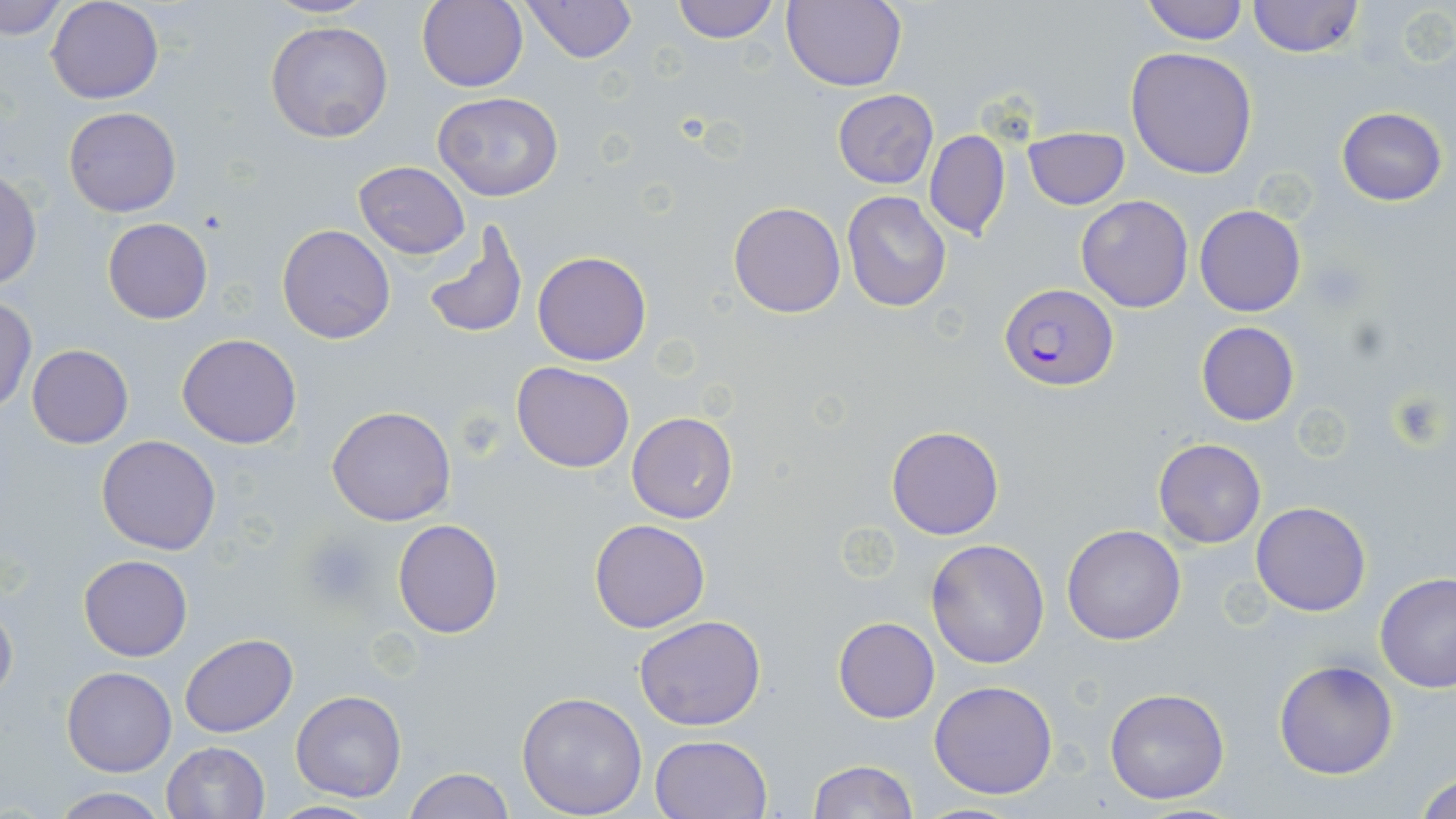
Summary:
  - Coordinate format: approximate bounding boxes as (x1,y1)-(x2,y2) corner pairs in pixels
  - Platelet locations: (1387,388)-(1451,450), (454,412)-(505,457), (303,534)-(375,606)
  - Uninfected red blood cell locations: (2,0)-(69,40), (46,0)-(164,104), (259,0)-(380,18), (415,0)-(529,90), (522,0)-(636,64), (672,0)-(780,44), (783,0)-(908,92), (1247,0)-(1363,58), (1140,1)-(1251,45), (265,20)-(393,144), (1126,47)-(1258,179), (832,90)-(939,188), (431,91)-(564,202), (64,106)-(181,217), (1335,107)-(1448,206), (1023,127)-(1130,210), (924,130)-(1010,241), (353,161)-(471,258), (0,170)-(43,289), (841,191)-(952,312), (1075,195)-(1194,312), (728,201)-(846,318), (1195,205)-(1305,316), (102,218)-(213,324), (420,219)-(529,342), (277,224)-(395,344), (532,249)-(652,366), (0,297)-(36,412), (1195,321)-(1300,425), (177,333)-(303,450), (26,344)-(133,448), (512,361)-(635,473), (326,405)-(457,526), (627,411)-(739,524), (885,425)-(1004,539), (97,435)-(221,555), (1153,437)-(1266,549), (1252,501)-(1371,616), (392,519)-(503,638), (590,519)-(711,632), (1061,525)-(1185,646), (926,538)-(1050,669), (78,554)-(192,661), (1374,572)-(1456,692), (0,597)-(18,709), (633,614)-(767,732), (833,616)-(939,723), (180,634)-(297,739), (1273,658)-(1398,779), (62,667)-(177,776), (929,680)-(1058,801), (1104,687)-(1231,805), (291,690)-(407,802), (516,692)-(648,818), (650,733)-(772,818), (161,741)-(270,819), (807,760)-(918,818), (402,768)-(514,819), (1414,769)-(1456,819), (49,787)-(168,819), (267,800)-(379,817), (910,801)-(1034,818)
  - Plasmodium falciparum-infected red blood cell locations: (1001,283)-(1120,391)
  - Slide-level diagnosis: Plasmodium falciparum
  - Field of view: single
  - Stain: May-Grünwald-Giemsa
  - Image size: 1456×819 pixels
  - Magnification: 1000x
  - Preparation: thin blood smear
  - Modality: optical microscopy